Describe the morphology of the red blood cells.
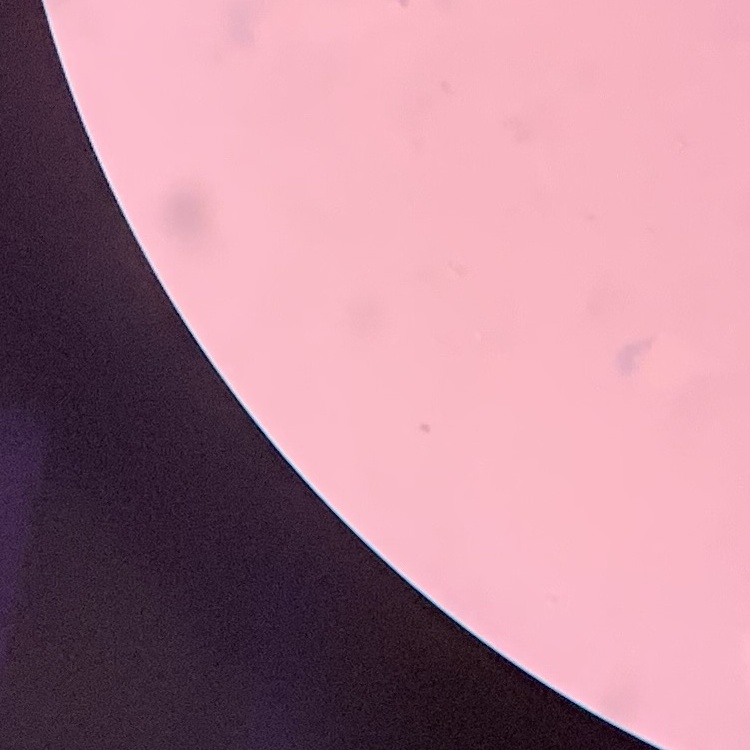

Rouleaux formation.

Summary:
  - Stain: Field's or Giemsa
  - Image type: one tile cut from a larger photomicrograph
  - Preparation: thin blood smear